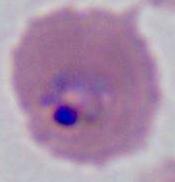 A Plasmodium parasite is shown. Photomicrograph. 400x or 1000x magnification.